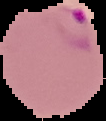
preparation = thin blood smear
malaria status = parasitized
image size = 106×121 pixels
image type = segmented cell region on a black background